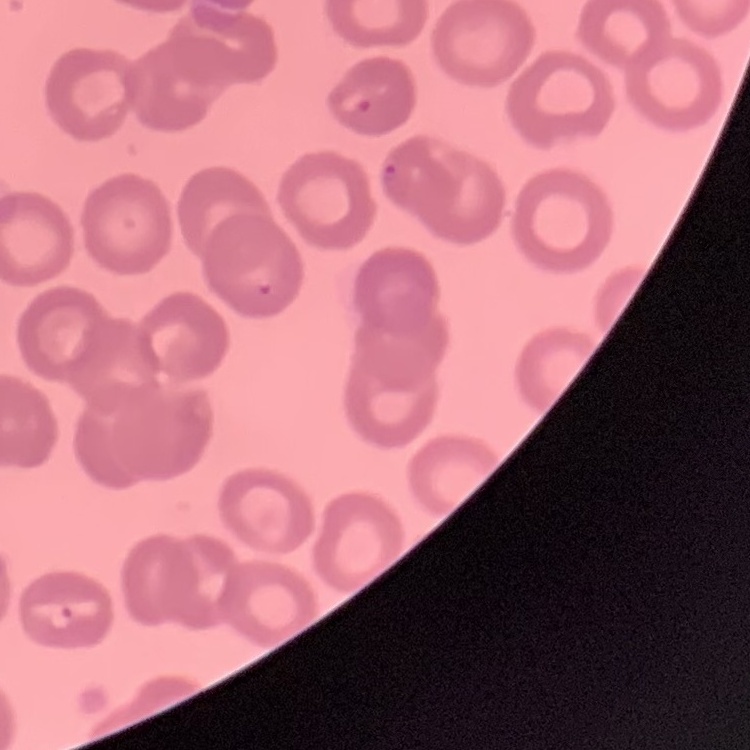
The red blood cells show no rouleaux formation. Stained with either Field's or Giemsa. Square crop of a larger photomicrograph. Thin blood smear.